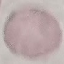
Result: negative for malaria parasites. Thin blood film. Giemsa stain. Photographed with a smartphone camera at the microscope eyepiece. Automatically extracted cell patch, resized to 64 × 64 pixels.